Locate every leukocyte (white blood cell).
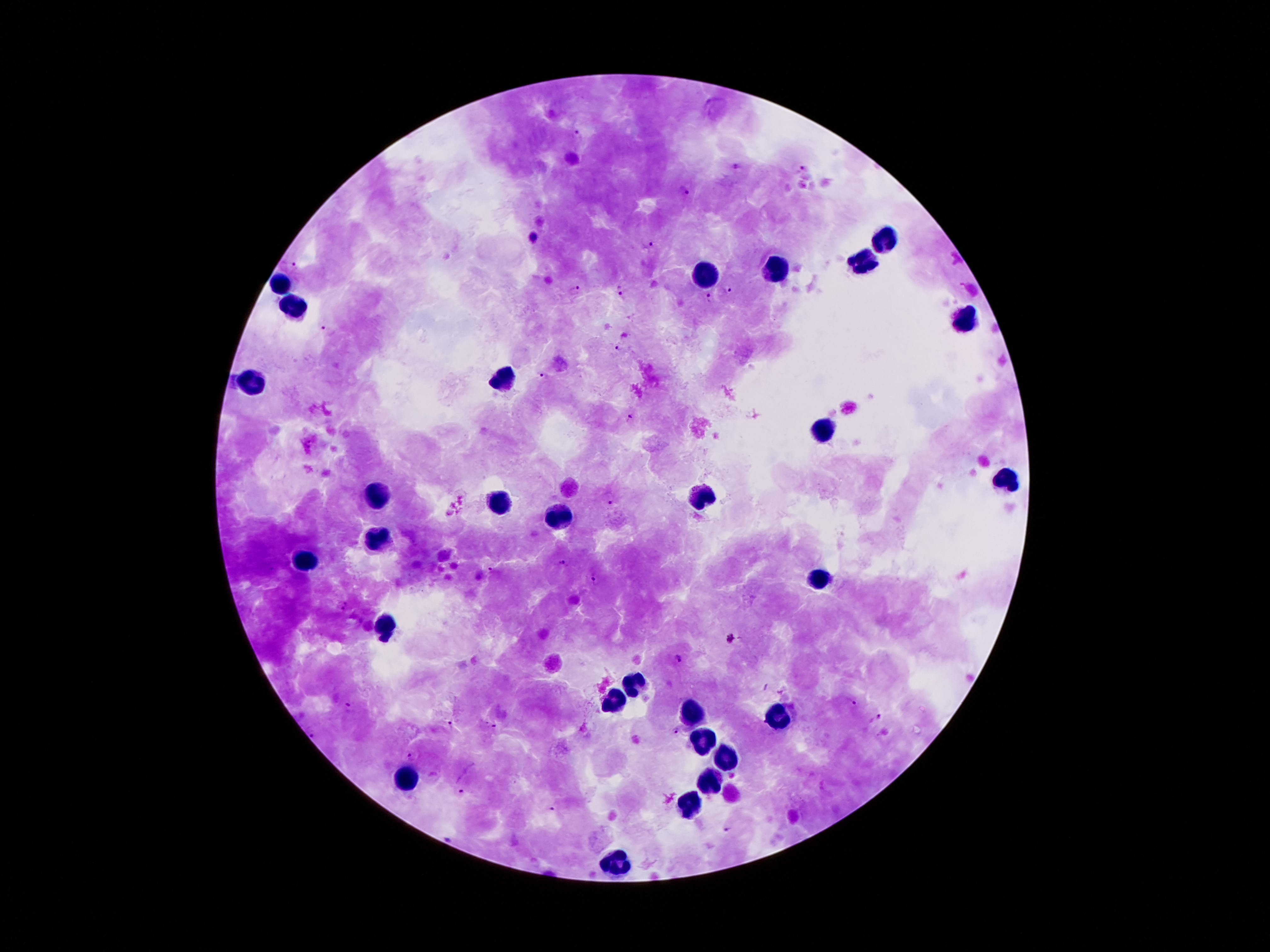
Approximate centers as {x, y} in pixels.
Leukocytes: {884, 241}, {866, 262}, {777, 273}, {706, 278}, {279, 288}, {294, 309}, {966, 322}, {499, 382}, {248, 383}, {821, 429}, {1006, 482}, {382, 494}, {701, 495}, {494, 503}, {558, 516}, {375, 541}, {309, 564}, {820, 578}, {383, 625}, {632, 684}, {614, 704}, {691, 717}, {770, 717}, {703, 742}, {728, 761}, {411, 780}, {708, 783}, {690, 809}, {619, 865}.

Plasmodium parasite locations: {577, 134}, {735, 167}, {802, 170}, {684, 192}, {650, 246}, {294, 267}, {572, 289}, {729, 290}, {620, 293}, {708, 298}, {329, 331}, {619, 347}, {541, 377}, {630, 416}, {610, 498}, {561, 563}, {594, 579}, {733, 640}, {677, 660}, {850, 702}, {876, 718}, {447, 723}, {494, 723}, {674, 731}, {411, 757}, {461, 791}, {551, 810}. Giemsa stain. One field from this slide. Thick peripheral-blood smear. Image is 1270×952 pixels. Patient malaria status: positive for Plasmodium falciparum. 100x magnification. Smartphone photograph taken through the microscope eyepiece.